Identify the preparation type.
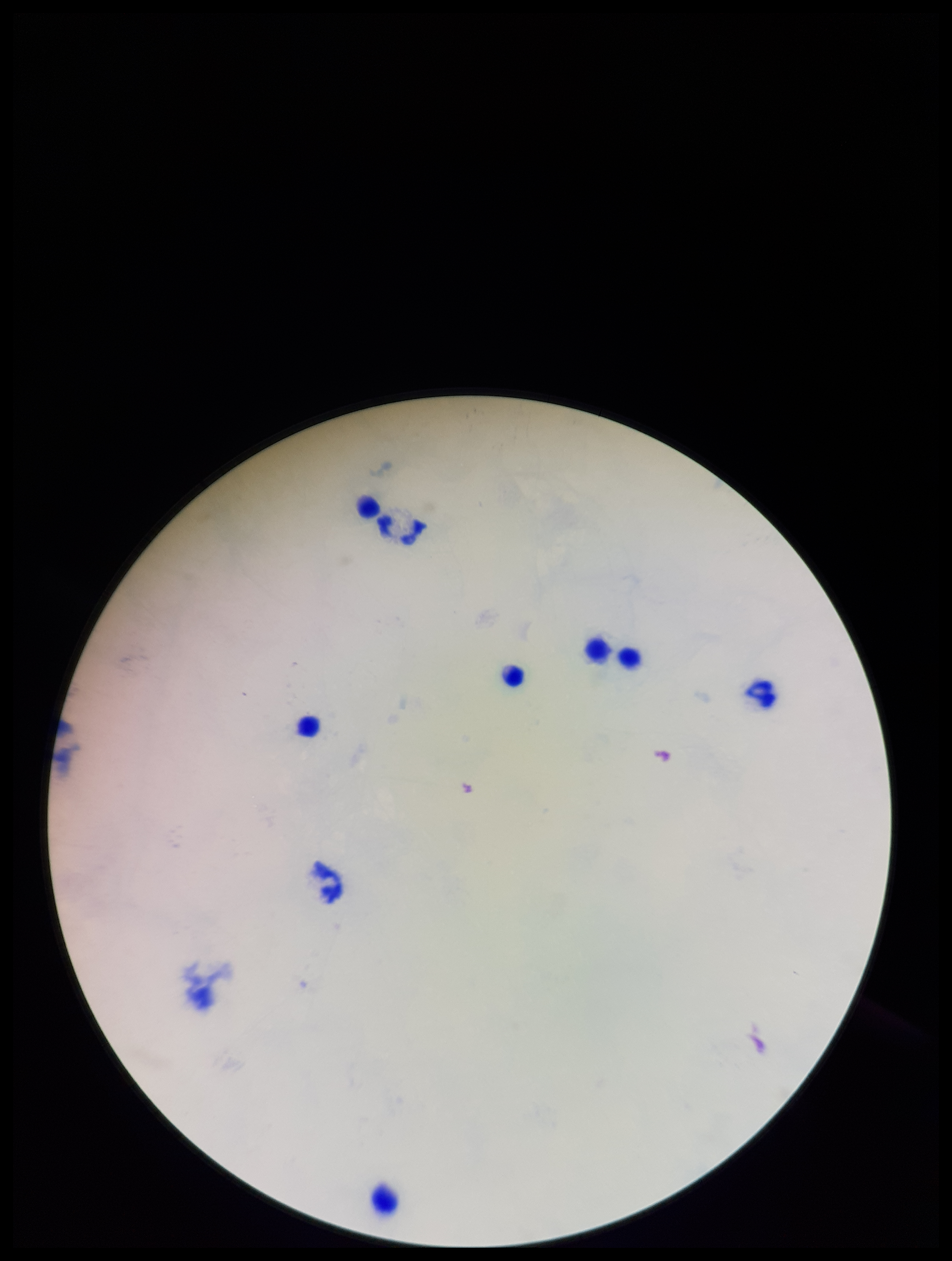
A thick smear.

Photographed through the microscope eyepiece with a smartphone camera. Leukocyte count: 9. Parasite count: 0. Plasmodium parasites: none detected. Patient malaria status: negative. One field from this slide. Stained with Giemsa. Image is 952×1261 pixels.